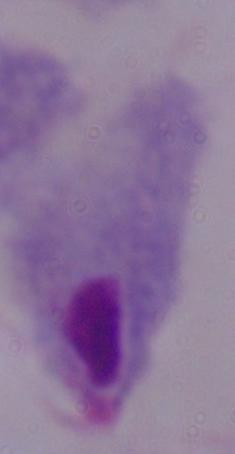
Summary:
  - Modality: micrograph
  - Identification: trichomonad
  - Magnification: 1000x